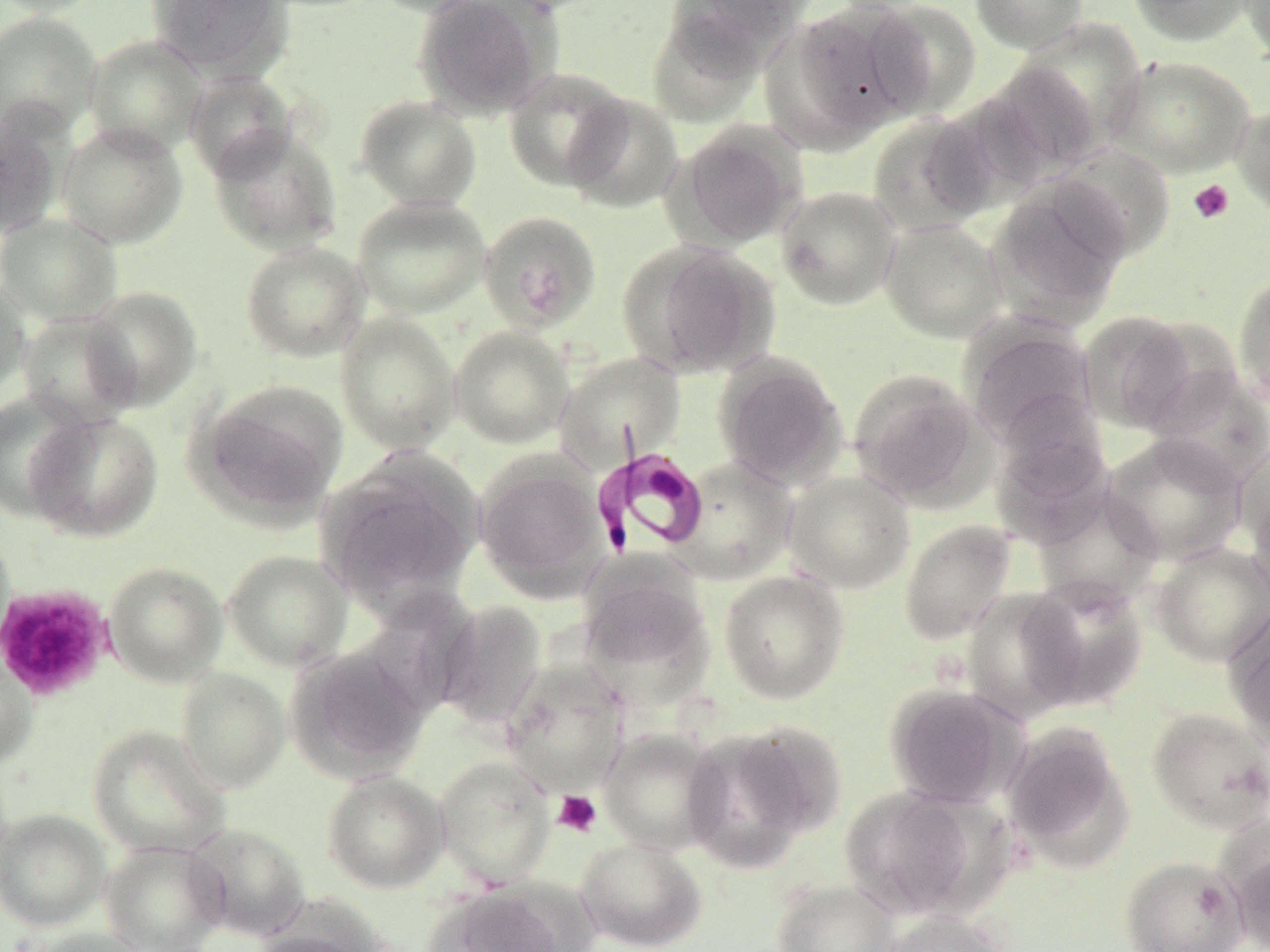
Summary:
  - Coordinate format: approximate bounding boxes as (x1,y1)-(x2,y2) corner pairs in pixels
  - Uninfected red blood cell locations: (0,0)-(103,17), (147,0)-(291,78), (369,0)-(491,18), (412,0)-(555,119), (667,0)-(807,63), (969,0)-(1090,54), (1128,0)-(1256,47), (1238,0)-(1270,65), (866,1)-(982,118), (778,3)-(925,144), (0,11)-(102,141), (647,12)-(766,128), (1011,19)-(1145,150), (84,34)-(206,157), (1106,54)-(1256,178), (982,61)-(1103,179), (503,67)-(632,191), (184,69)-(297,181), (562,92)-(684,213), (354,94)-(482,210), (1232,102)-(1270,222), (0,110)-(64,240), (867,114)-(996,236), (56,121)-(189,249), (673,122)-(807,250), (208,125)-(343,255), (1050,143)-(1177,262), (988,179)-(1131,325), (775,186)-(902,311), (352,196)-(490,318), (478,210)-(602,333), (0,213)-(122,326), (879,218)-(1007,342), (240,240)-(370,362), (620,241)-(779,379), (1233,272)-(1270,408), (0,275)-(31,399), (81,285)-(202,411), (1078,310)-(1205,433), (16,312)-(138,429), (335,312)-(460,454), (963,320)-(1097,445), (449,326)-(573,448), (554,352)-(685,465), (713,353)-(849,489), (848,368)-(988,511), (1146,369)-(1270,487), (192,380)-(347,525), (0,390)-(94,521), (991,398)-(1113,525), (25,411)-(163,541), (1100,432)-(1248,566), (1233,436)-(1270,558), (316,450)-(483,608), (473,454)-(610,599), (670,455)-(795,584), (783,470)-(915,594), (1245,478)-(1270,609), (1032,486)-(1164,608), (898,519)-(1017,645), (0,526)-(16,660), (1150,541)-(1270,667), (223,549)-(351,671), (103,560)-(227,687), (576,563)-(714,691), (718,569)-(850,704), (1020,576)-(1148,711), (961,587)-(1088,722), (434,599)-(547,730), (1223,603)-(1270,747), (286,645)-(430,781), (0,650)-(38,772), (500,662)-(630,796), (176,668)-(290,792), (883,682)-(1025,809), (1146,706)-(1270,834), (681,723)-(834,872), (1001,723)-(1135,868), (87,725)-(229,858), (598,728)-(726,855), (434,755)-(555,888), (322,770)-(449,893), (838,785)-(987,920), (0,808)-(110,931), (184,822)-(311,941), (575,837)-(707,951), (99,839)-(229,951), (1230,841)-(1270,952), (1120,855)-(1249,952), (772,879)-(900,952), (424,885)-(575,952), (877,910)-(1014,952), (26,927)-(154,952), (249,931)-(375,952)
  - Platelet locations: (1188,179)-(1235,224), (0,584)-(113,702), (553,790)-(602,837)
  - Trypanosoma brucei locations: (592,444)-(709,556)
  - Slide-level diagnosis: Trypanosoma brucei
  - Magnification: 1000x
  - Preparation: thin blood film
  - Modality: optical microscopy
  - Image size: 1270×952 pixels
  - Field of view: single
  - Stain: May-Grünwald-Giemsa